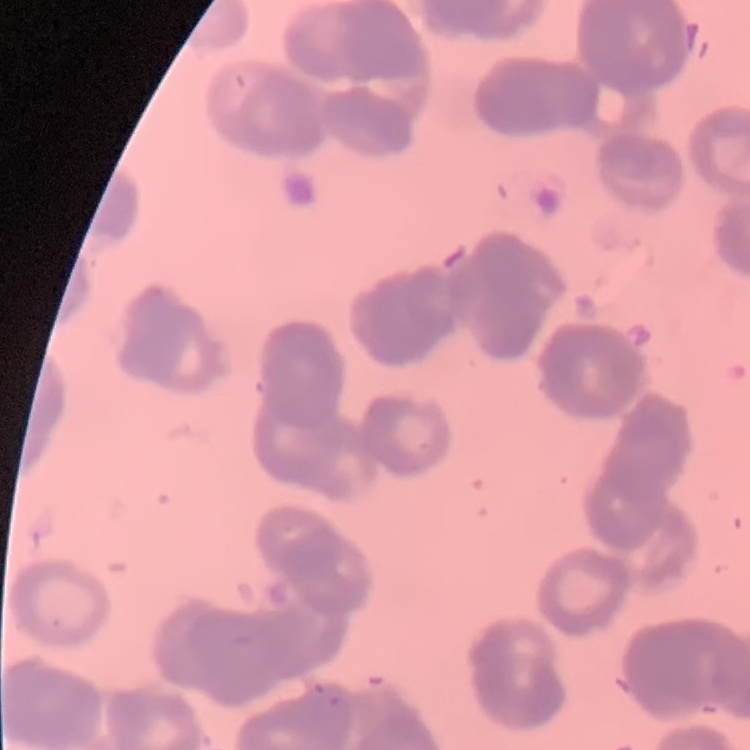
red blood cell morphology = rouleaux formation
stain = Field's or Giemsa
image type = square crop of a larger photomicrograph
preparation = thin peripheral smear